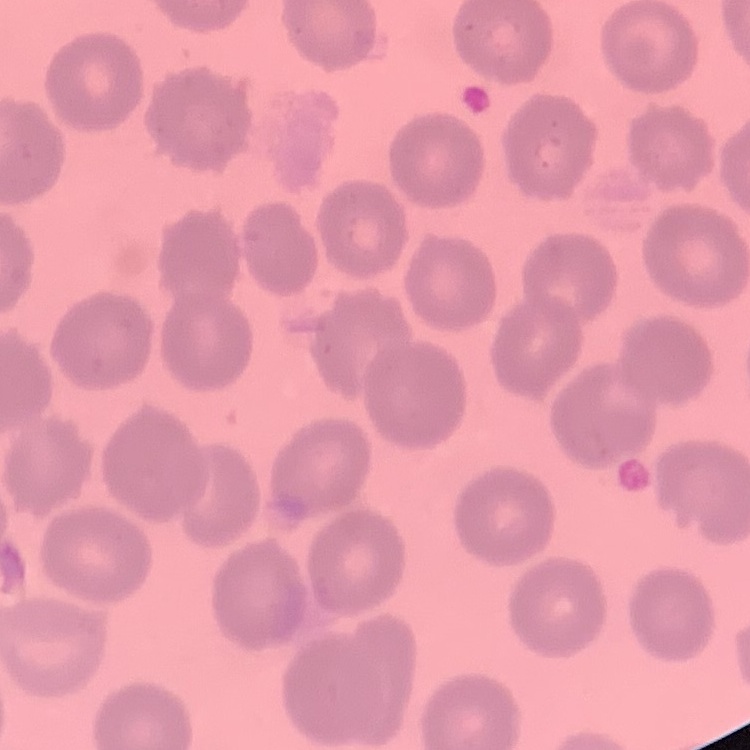
red blood cell morphology = no rouleaux formation
preparation = thin blood film
stain = Field's or Giemsa
image type = square crop of a larger photomicrograph